State which parasite is depicted.
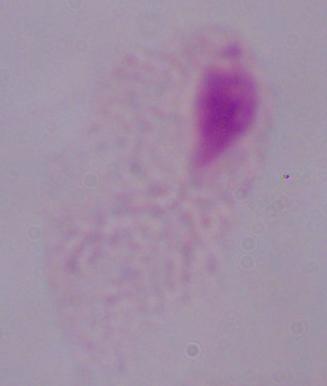
This is a trichomonad.

magnification: 1000x
modality: micrograph